Comment on the morphology of the red blood cells.
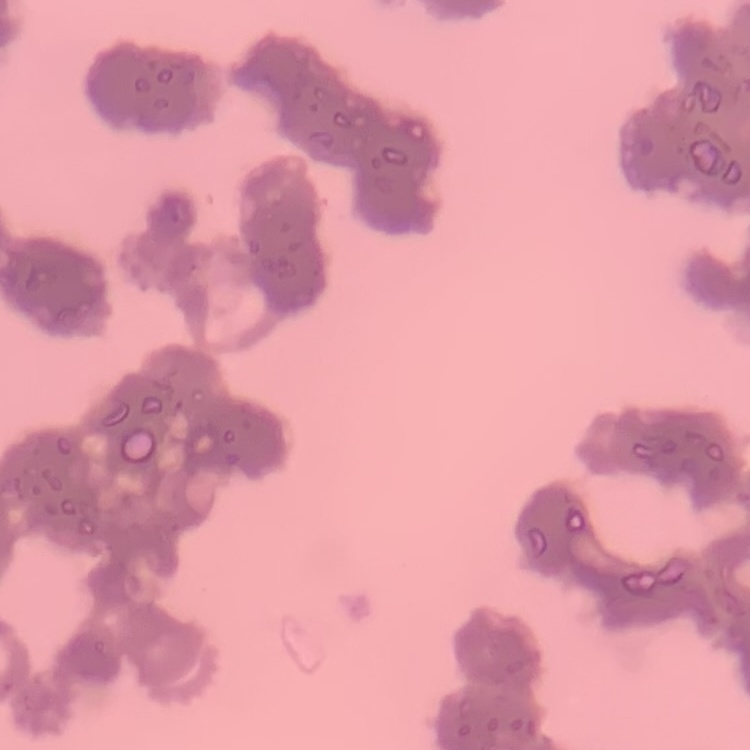
They show rouleaux formation.

preparation = thin peripheral smear
stain = Field's or Giemsa
image type = square crop of a larger photomicrograph